Assess this cell for malaria.
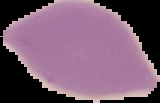
It is uninfected.

Summary:
  - Image size: 160×103 pixels
  - Preparation: thin blood film
  - Image type: cell region segmented out of the field of view; surrounding area masked to black